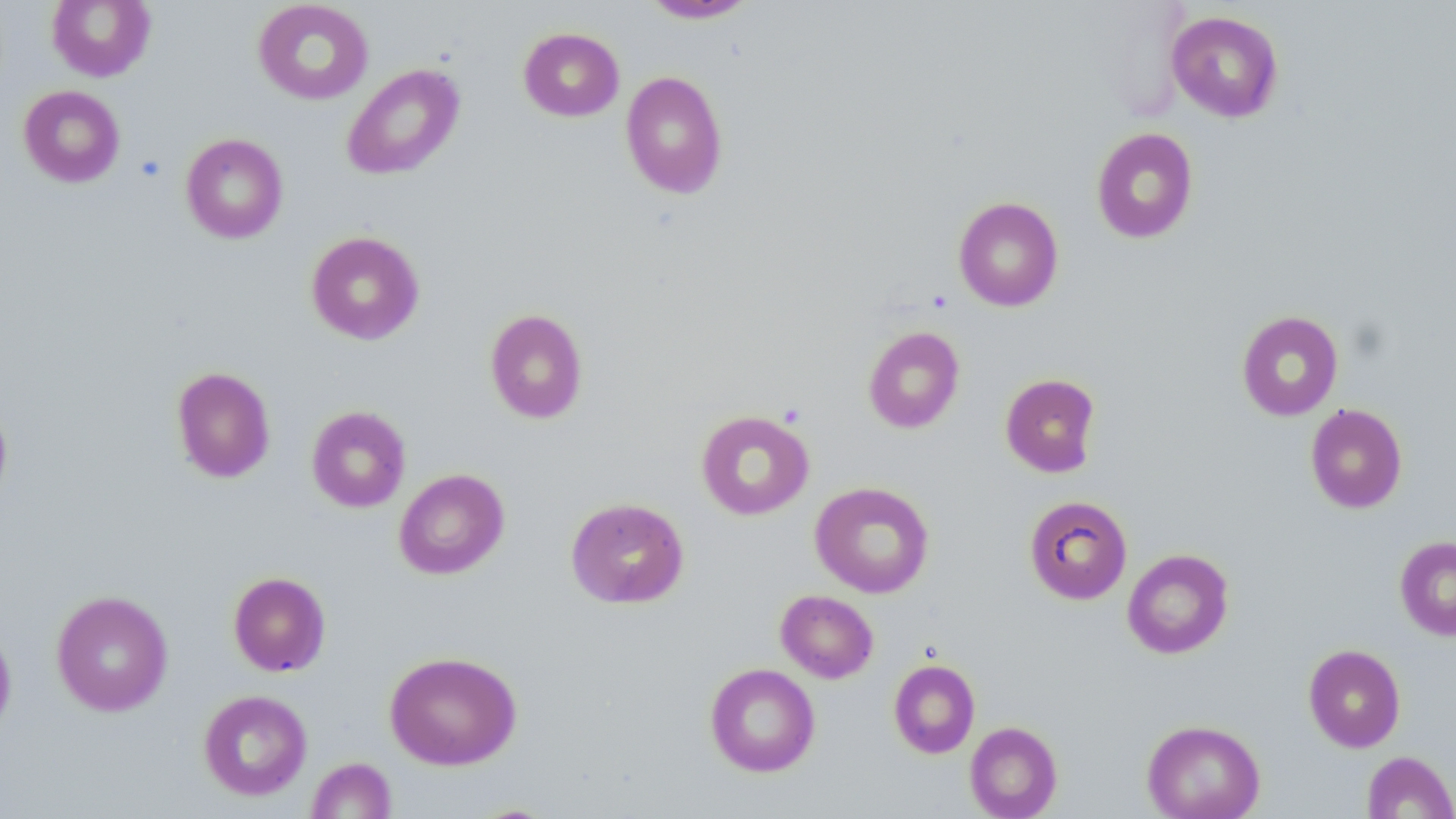

Summary:
  - Coordinate format: approximate bounding boxes as (x1,y1)-(x2,y2) corner pairs in pixels
  - Uninfected red blood cell locations: (46,0)-(156,82), (252,0)-(373,105), (640,1)-(757,23), (1166,10)-(1284,123), (518,27)-(624,121), (341,63)-(465,182), (620,70)-(728,199), (18,85)-(125,188), (1091,127)-(1199,243), (181,133)-(288,243), (953,196)-(1064,311), (306,230)-(425,345), (484,308)-(588,424), (1236,310)-(1343,421), (863,326)-(965,434), (171,366)-(276,483), (1000,373)-(1101,477), (0,396)-(13,513), (1305,403)-(1408,514), (306,405)-(411,512), (695,410)-(815,520), (394,468)-(509,580), (810,481)-(934,598), (1024,495)-(1132,605), (565,497)-(689,609), (1394,536)-(1456,640), (1122,548)-(1234,659), (228,571)-(331,677), (51,590)-(174,716), (776,590)-(878,683), (0,619)-(17,742), (1303,644)-(1406,752), (384,651)-(522,770), (888,659)-(980,758), (705,663)-(820,777), (198,689)-(312,800), (1142,719)-(1265,819), (964,721)-(1063,818), (1361,750)-(1456,818), (306,757)-(397,818)
  - Slide-level diagnosis: negative for blood parasites
  - Magnification: 1000x
  - Modality: light microscopy
  - Preparation: thin blood film
  - Image size: 1456×819 pixels
  - Field of view: one of a larger specimen
  - Stain: May-Grünwald-Giemsa